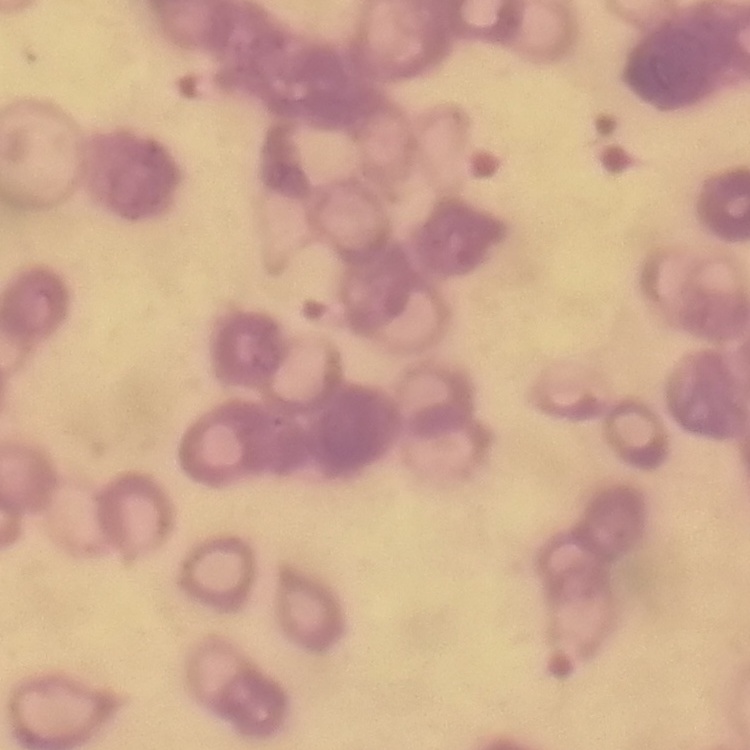

red_blood_cell_morphology: rouleaux formation
image_type: one tile cut from a larger photomicrograph
stain: Field's or Giemsa
preparation: thin peripheral smear